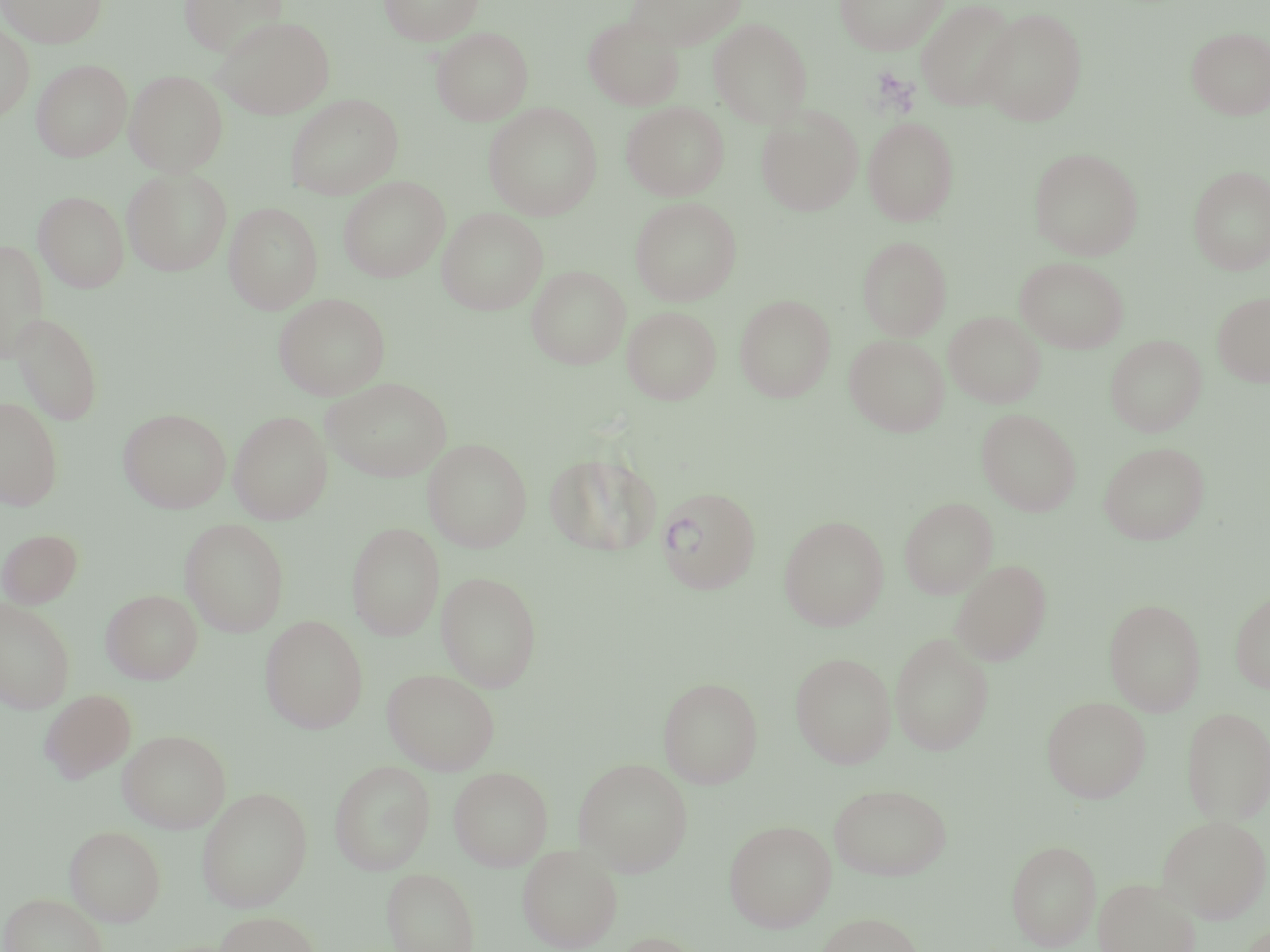
Summary:
  - Coordinate format: approximate bounding boxes as (x1, y1, x2, y2) in pixels
  - Uninfected red blood cell locations: (0, 0, 108, 48), (175, 0, 287, 57), (380, 0, 484, 46), (624, 0, 746, 50), (834, 0, 948, 55), (916, 0, 1020, 112), (977, 7, 1088, 126), (212, 15, 335, 119), (583, 16, 683, 110), (708, 18, 813, 127), (0, 22, 35, 122), (432, 27, 533, 125), (1186, 27, 1270, 120), (32, 59, 132, 161), (125, 69, 228, 177), (286, 94, 403, 200), (622, 101, 729, 200), (483, 102, 602, 220), (756, 106, 863, 216), (863, 116, 959, 225), (1029, 147, 1144, 260), (1188, 165, 1270, 274), (122, 167, 233, 276), (338, 176, 449, 282), (33, 190, 129, 293), (630, 197, 742, 305), (223, 202, 322, 314), (437, 208, 548, 315), (858, 236, 951, 340), (0, 240, 48, 363), (1015, 257, 1129, 353), (527, 265, 630, 369), (1213, 291, 1270, 387), (274, 293, 390, 400), (734, 294, 836, 401), (622, 305, 722, 405), (944, 311, 1045, 408), (10, 312, 104, 426), (844, 334, 950, 436), (1105, 334, 1207, 436), (322, 377, 453, 482), (0, 396, 64, 510), (118, 408, 231, 513), (976, 408, 1081, 515), (229, 410, 332, 524), (423, 438, 532, 552), (1098, 442, 1210, 545), (545, 452, 661, 556), (899, 497, 998, 598), (779, 515, 889, 630), (179, 518, 290, 636), (346, 523, 444, 640), (0, 528, 84, 608), (950, 559, 1053, 665), (436, 571, 542, 691), (101, 589, 203, 684), (1230, 589, 1270, 695), (1104, 598, 1206, 715), (0, 599, 76, 713), (260, 615, 368, 733), (889, 632, 994, 756), (790, 652, 896, 768), (382, 668, 500, 775), (657, 676, 763, 788), (39, 689, 137, 784), (1041, 696, 1151, 803), (1181, 706, 1270, 824), (117, 729, 232, 833), (573, 758, 693, 875), (329, 760, 435, 875), (448, 766, 553, 871), (828, 783, 952, 881), (196, 787, 313, 912), (1157, 815, 1269, 921), (723, 819, 837, 932), (64, 825, 166, 926), (1006, 840, 1101, 950), (517, 844, 624, 952), (381, 867, 479, 952), (1093, 878, 1202, 952), (1, 892, 108, 952), (214, 911, 323, 952), (814, 912, 926, 952), (606, 931, 709, 952)
  - Plasmodium vivax-infected red blood cell locations: (655, 486, 761, 594)
  - Slide-level diagnosis: Plasmodium vivax
  - Stain: May-Grünwald-Giemsa
  - Preparation: thin blood film
  - Modality: optical microscopy
  - Magnification: 1000x
  - Image size: 1270×952 pixels
  - Field of view: one of a larger specimen